Classify this cell by malaria status.
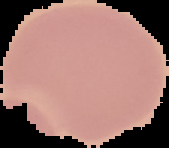

Uninfected.

Image is 169×148 pixels. Segmented cell region on a black background. From a thin blood film.